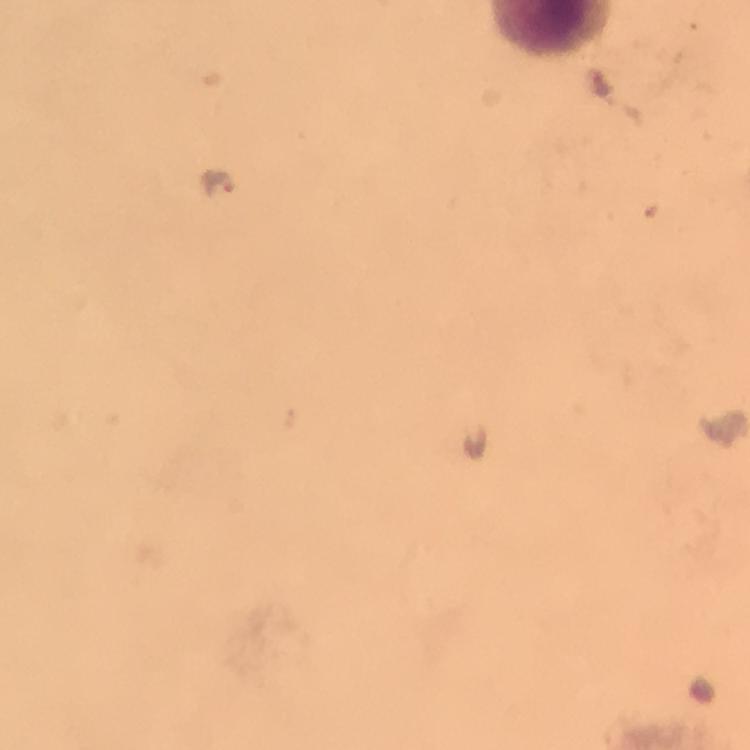

{
  "image_size": "750×750 pixels",
  "magnification": "100x",
  "malaria_parasite_locations": "approximate object centers, in pixels from the top-left corner: (x=218, y=184)",
  "stain": "Giemsa",
  "cropped_from": "one field of view",
  "immersion_oil": "applied",
  "context": "from a diagnostic examination for malaria",
  "preparation": "thick smear",
  "capture": "smartphone camera through the microscope"
}